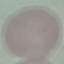
malaria status = uninfected
preparation = thin blood smear
stain = Giemsa
capture = smartphone through the microscope eyepiece
image type = automatically extracted cell patch, resized to 64 × 64 pixels